Name the parasite shown.
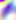

Toxoplasma gondii.

Photomicrograph. 400x magnification.